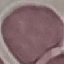
malaria status = uninfected
stain = Giemsa
image type = automatically extracted cell patch, resized to 64 × 64 pixels
preparation = thin blood film
capture = smartphone camera at the microscope eyepiece